Locate every Plasmodium parasite.
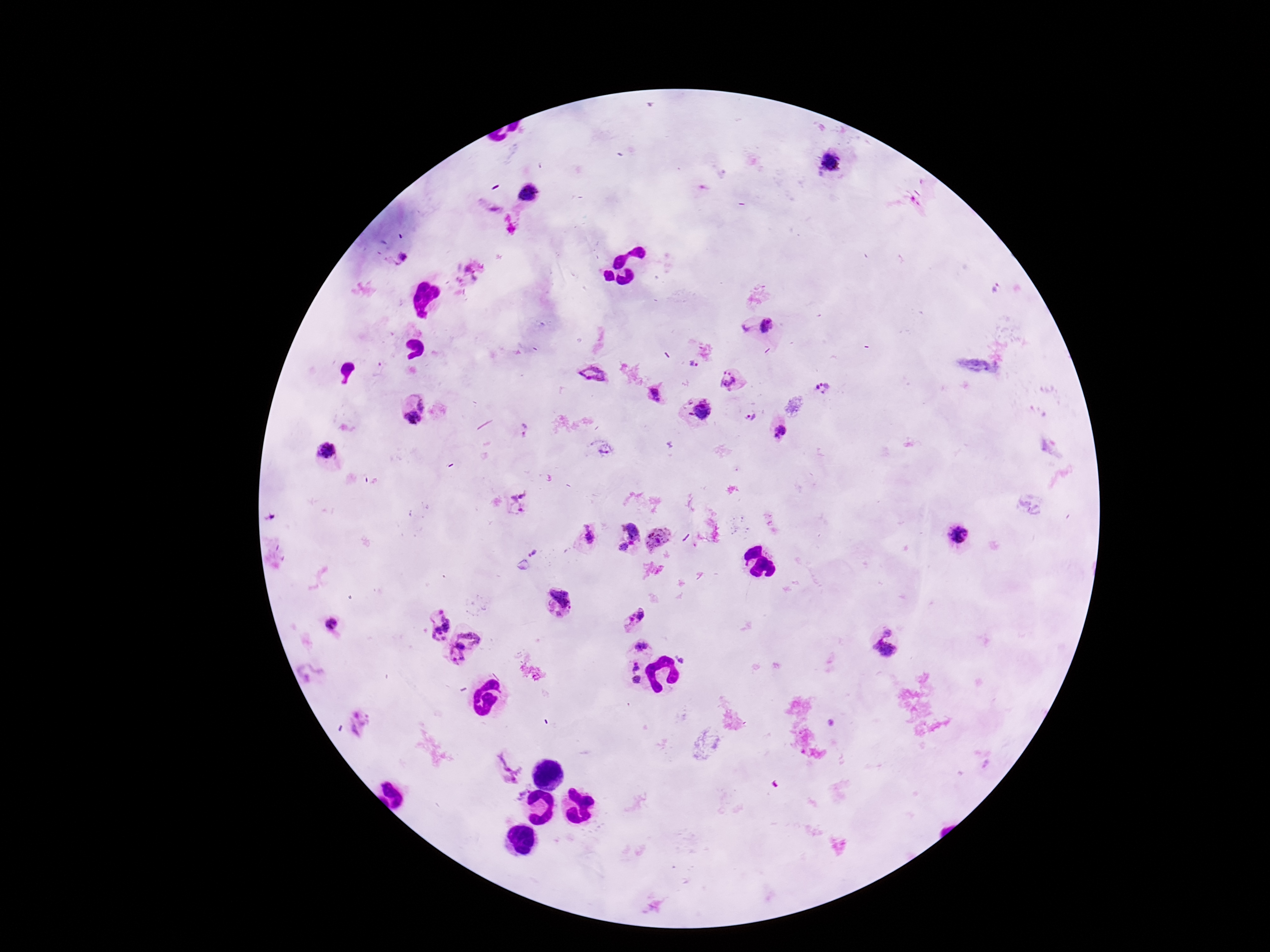
Approximate centers as (x, y) in pixels.
Plasmodium parasites: (832, 166), (529, 195), (400, 257), (757, 326), (691, 366), (590, 374), (733, 381), (822, 388), (656, 394), (699, 410), (414, 411), (750, 417), (523, 430), (781, 431), (325, 455), (522, 506), (587, 537), (623, 537), (961, 537), (659, 538), (534, 554), (560, 600), (631, 617), (438, 623), (336, 631), (467, 645), (641, 646), (883, 646), (680, 660), (633, 669), (312, 672), (638, 681), (358, 723), (505, 767), (522, 796).

Thick blood smear. Giemsa-stained preparation. Patient malaria status: positive. Photographed through the microscope eyepiece with a smartphone camera. Image is 1270×952 pixels. 100x magnification. One field from this slide.